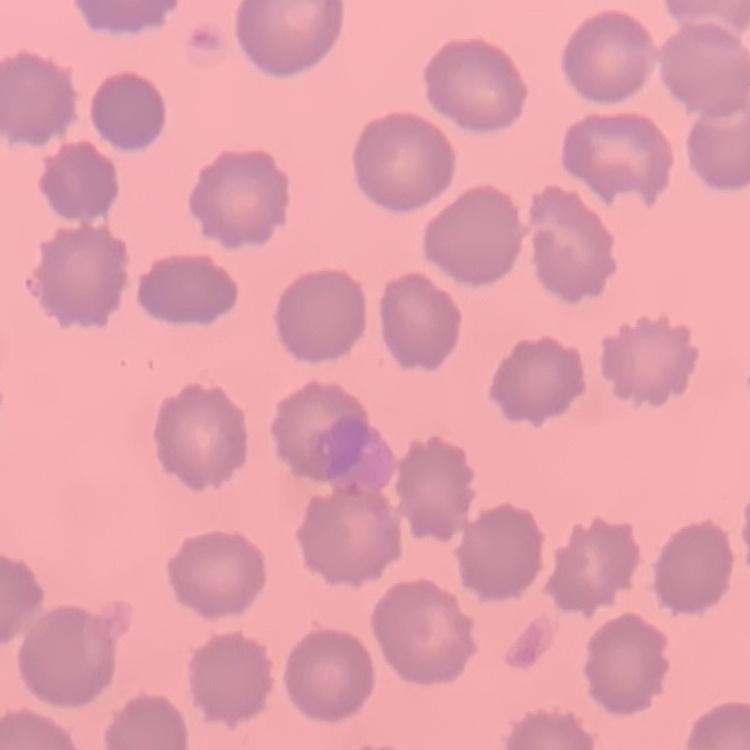
Summary:
  - Red blood cell morphology: no rouleaux formation
  - Stain: Field's or Giemsa
  - Image type: square crop of a larger photomicrograph
  - Preparation: thin blood film